Outline each blood parasite and name the species.
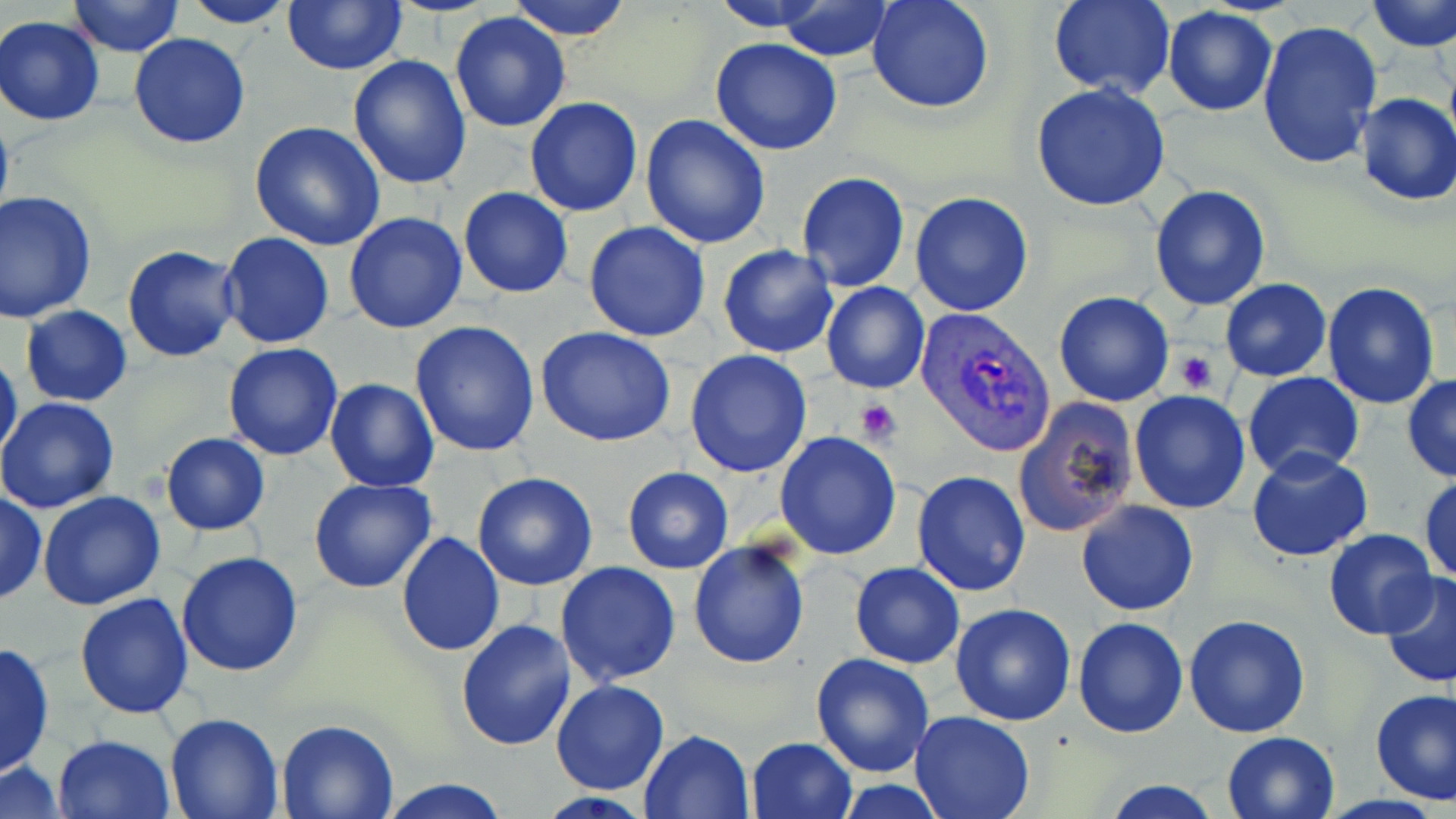
Approximate bounding boxes as named x1/y1/x2/y2 corners in pixels.
Plasmodium vivax-infected red blood cells: (x1=912, y1=305, x2=1061, y2=457).
No Plasmodium falciparum, Plasmodium ovale, Plasmodium malariae, Babesia divergens, or Trypanosoma brucei observed.

Platelet locations: (x1=1176, y1=351, x2=1217, y2=394), (x1=855, y1=399, x2=900, y2=446). Uninfected red blood cell locations: (x1=65, y1=0, x2=186, y2=55), (x1=181, y1=0, x2=297, y2=28), (x1=508, y1=0, x2=633, y2=42), (x1=707, y1=0, x2=842, y2=32), (x1=778, y1=0, x2=895, y2=61), (x1=866, y1=0, x2=995, y2=115), (x1=1047, y1=0, x2=1175, y2=99), (x1=1366, y1=0, x2=1456, y2=53), (x1=282, y1=1, x2=407, y2=75), (x1=1162, y1=6, x2=1278, y2=118), (x1=449, y1=11, x2=572, y2=132), (x1=1, y1=16, x2=106, y2=125), (x1=1257, y1=19, x2=1383, y2=169), (x1=128, y1=33, x2=252, y2=148), (x1=710, y1=38, x2=841, y2=155), (x1=347, y1=55, x2=473, y2=191), (x1=1030, y1=83, x2=1171, y2=212), (x1=1352, y1=94, x2=1456, y2=206), (x1=524, y1=96, x2=642, y2=216), (x1=639, y1=115, x2=770, y2=249), (x1=248, y1=121, x2=386, y2=251), (x1=796, y1=171, x2=910, y2=292), (x1=796, y1=182, x2=1030, y2=303), (x1=1149, y1=185, x2=1271, y2=311), (x1=459, y1=188, x2=573, y2=298), (x1=0, y1=191, x2=99, y2=323), (x1=909, y1=191, x2=1034, y2=317), (x1=343, y1=211, x2=469, y2=334), (x1=583, y1=221, x2=711, y2=341), (x1=218, y1=231, x2=336, y2=348), (x1=717, y1=244, x2=838, y2=358), (x1=122, y1=245, x2=243, y2=363), (x1=1220, y1=279, x2=1331, y2=382), (x1=821, y1=280, x2=930, y2=394), (x1=1321, y1=280, x2=1440, y2=410), (x1=1053, y1=290, x2=1177, y2=407), (x1=20, y1=305, x2=132, y2=407), (x1=409, y1=320, x2=541, y2=458), (x1=535, y1=326, x2=676, y2=447), (x1=222, y1=342, x2=343, y2=461), (x1=0, y1=346, x2=23, y2=467), (x1=684, y1=350, x2=813, y2=478), (x1=1242, y1=371, x2=1365, y2=479), (x1=1402, y1=375, x2=1456, y2=483), (x1=324, y1=378, x2=440, y2=492), (x1=1129, y1=390, x2=1250, y2=514), (x1=0, y1=395, x2=121, y2=513), (x1=1015, y1=398, x2=1140, y2=538), (x1=774, y1=431, x2=903, y2=560), (x1=161, y1=433, x2=270, y2=536), (x1=1246, y1=449, x2=1374, y2=563), (x1=621, y1=467, x2=734, y2=573), (x1=912, y1=470, x2=1032, y2=595), (x1=472, y1=472, x2=599, y2=591), (x1=1418, y1=474, x2=1455, y2=584), (x1=309, y1=478, x2=437, y2=593), (x1=0, y1=489, x2=47, y2=606), (x1=39, y1=490, x2=165, y2=610), (x1=1075, y1=500, x2=1200, y2=618), (x1=1322, y1=529, x2=1437, y2=640), (x1=395, y1=531, x2=505, y2=657), (x1=688, y1=539, x2=813, y2=670), (x1=176, y1=551, x2=305, y2=677), (x1=554, y1=561, x2=682, y2=687), (x1=848, y1=562, x2=964, y2=668), (x1=1379, y1=569, x2=1456, y2=688), (x1=75, y1=591, x2=194, y2=720), (x1=949, y1=604, x2=1077, y2=726), (x1=1184, y1=615, x2=1310, y2=737), (x1=1074, y1=617, x2=1189, y2=738), (x1=456, y1=620, x2=577, y2=753), (x1=0, y1=639, x2=55, y2=780), (x1=810, y1=652, x2=936, y2=777), (x1=551, y1=679, x2=670, y2=796), (x1=1370, y1=688, x2=1456, y2=803), (x1=910, y1=709, x2=1036, y2=819), (x1=166, y1=710, x2=283, y2=817), (x1=274, y1=718, x2=402, y2=818), (x1=640, y1=729, x2=755, y2=818), (x1=1222, y1=731, x2=1341, y2=819), (x1=52, y1=733, x2=176, y2=819), (x1=746, y1=736, x2=856, y2=819), (x1=1, y1=761, x2=66, y2=818), (x1=381, y1=777, x2=509, y2=818), (x1=1099, y1=777, x2=1225, y2=818), (x1=832, y1=780, x2=950, y2=816). Slide-level diagnosis: Plasmodium vivax. May-Grünwald-Giemsa stain. Image is 1456×819 pixels. 1000x magnification. Thin blood smear. Optical microscopy. Single field of view.